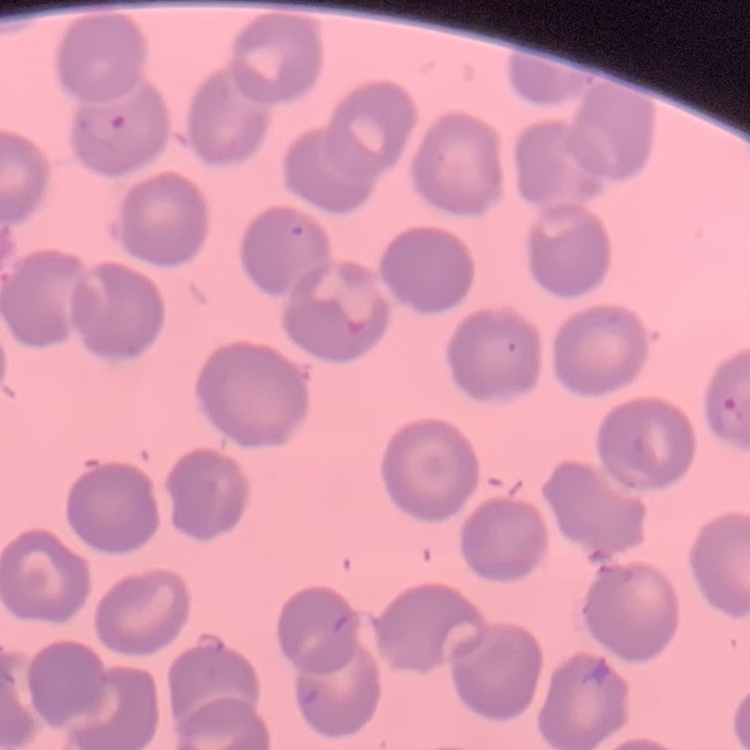

Summary:
  - Red blood cell morphology: no rouleaux formation
  - Stain: Field's or Giemsa
  - Image type: square crop of a larger photomicrograph
  - Preparation: thin blood smear